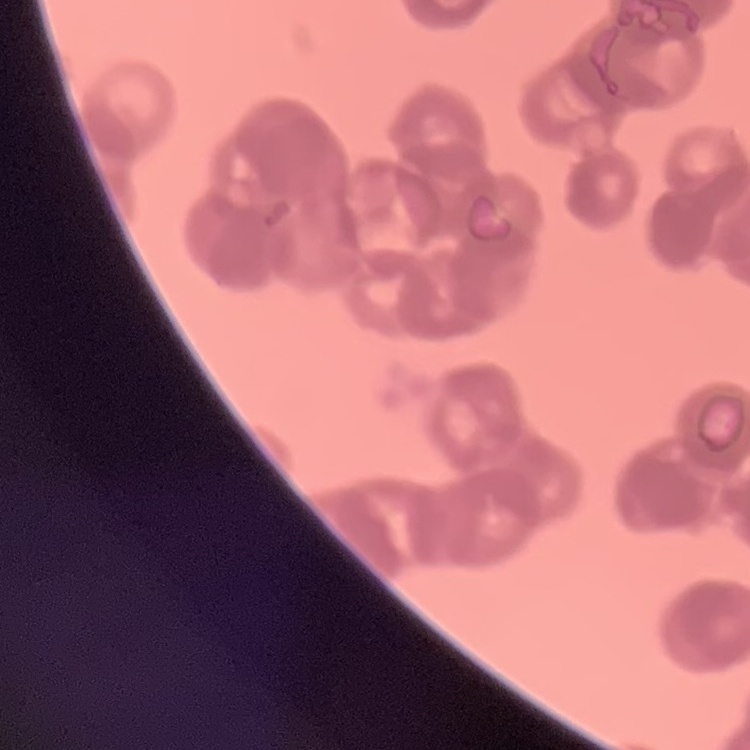

erythrocyte_morphology: rouleaux formation
image_type: square crop of a larger photomicrograph
stain: Field's or Giemsa
preparation: thin blood smear